Describe the morphology of the red blood cells.
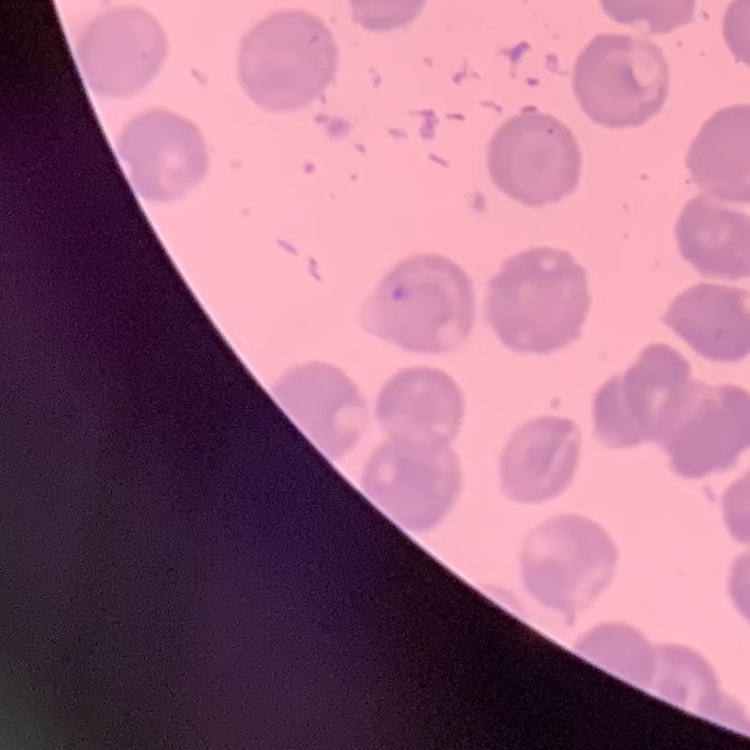
No rouleaux formation.

Summary:
  - Image type: one tile cut from a larger photomicrograph
  - Preparation: thin blood film
  - Stain: Field's or Giemsa